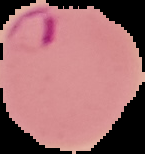

image_type: segmented cell region on a black background
malaria_status: parasitized
preparation: thin blood film
image_size: 145×154 pixels